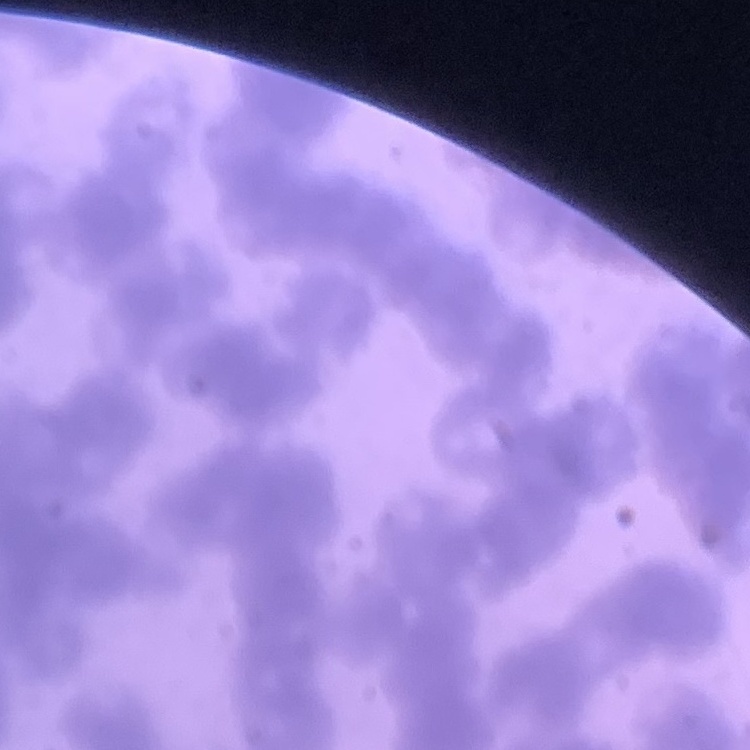 The red blood cells exhibit rouleaux formation. Stained with either Field's or Giemsa. Thin blood film. One tile cut from a larger photomicrograph.